Give the preparation type.
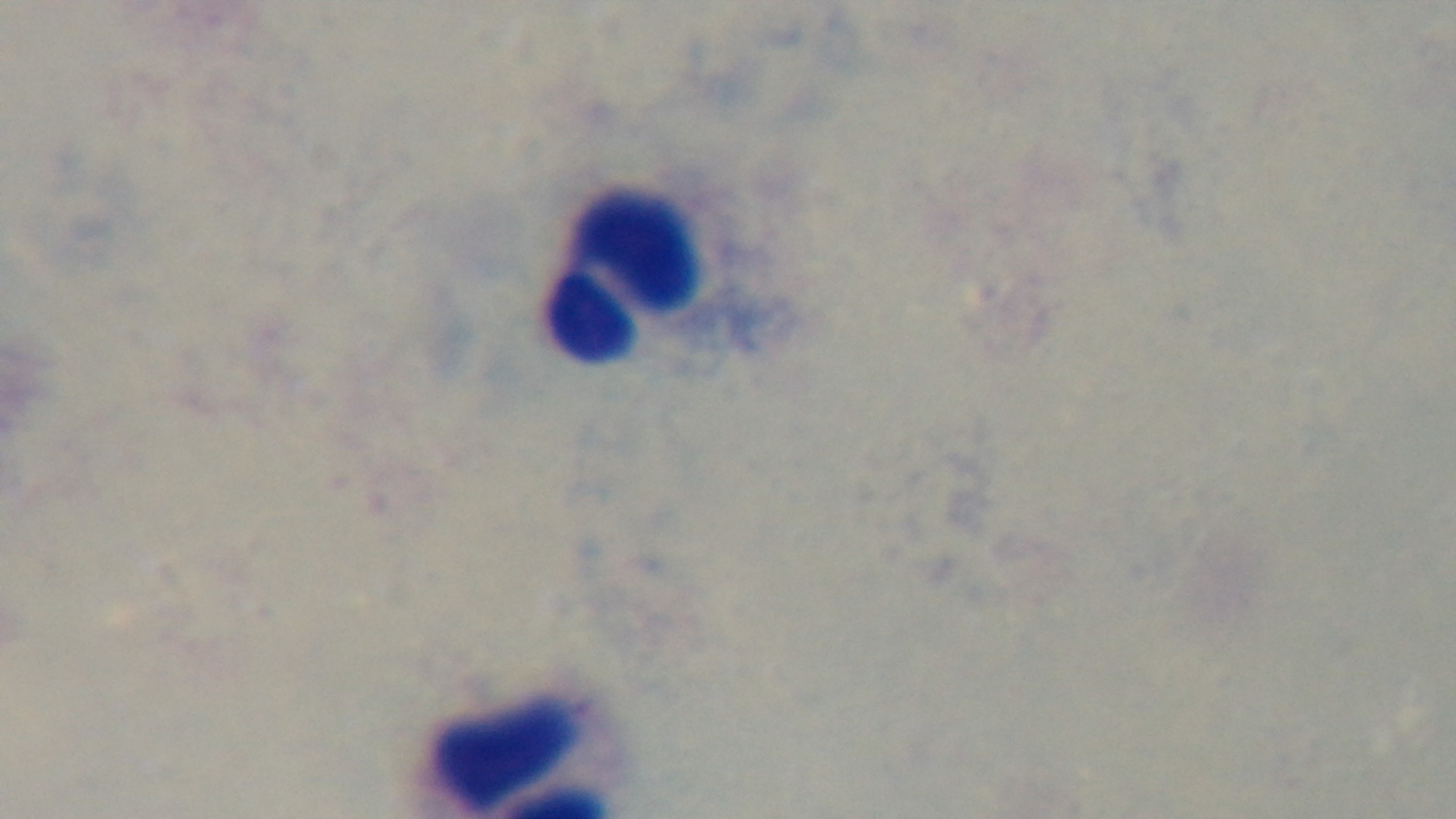

A thick smear.

field of view = single
objective = 100x oil immersion
modality = light microscopy
capture = mounted 4K digital camera
malaria status = uninfected
stain = Giemsa